Classify this cell by malaria status.
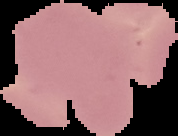

It is uninfected.

{
  "preparation": "thin blood film",
  "image_size": "178×136 pixels",
  "image_type": "segmented cell region with the area outside set to black"
}